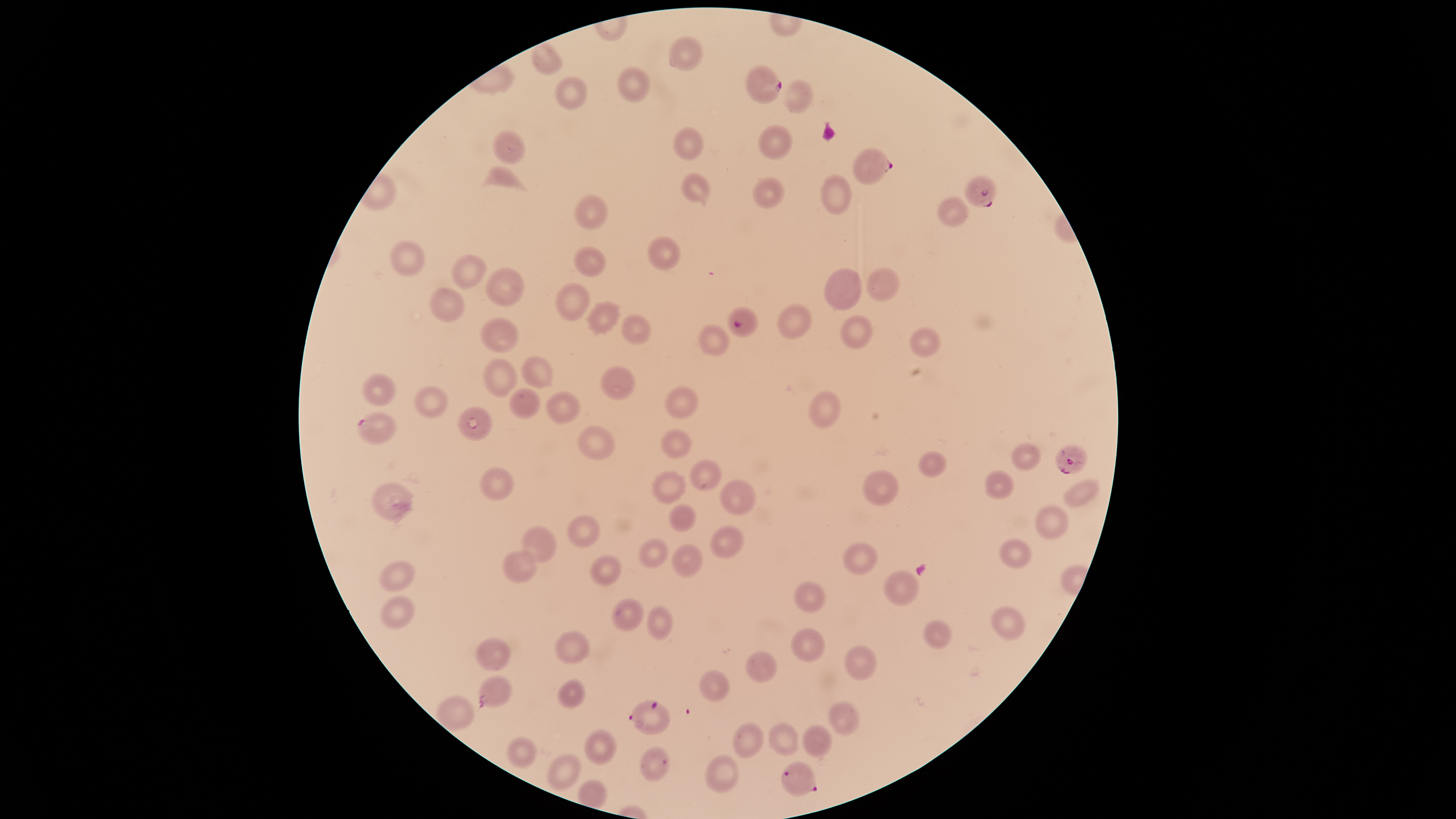

Approximate bounding boxes, in pixels from the top-left corner. Parasitized red blood cells: (left=745, top=64, right=782, bottom=104), (left=852, top=147, right=893, bottom=185), (left=964, top=175, right=997, bottom=207), (left=727, top=306, right=758, bottom=337), (left=357, top=411, right=397, bottom=445), (left=1054, top=444, right=1088, bottom=475), (left=478, top=676, right=512, bottom=708), (left=628, top=699, right=670, bottom=735), (left=781, top=762, right=817, bottom=797). Uninfected red blood cells: (left=668, top=36, right=703, bottom=70), (left=531, top=44, right=562, bottom=75), (left=616, top=66, right=651, bottom=102), (left=554, top=76, right=588, bottom=110), (left=782, top=78, right=815, bottom=114), (left=757, top=124, right=793, bottom=160), (left=671, top=127, right=706, bottom=160), (left=492, top=129, right=524, bottom=163), (left=479, top=165, right=531, bottom=193), (left=681, top=172, right=711, bottom=202), (left=820, top=174, right=852, bottom=215), (left=751, top=177, right=785, bottom=209), (left=573, top=194, right=608, bottom=230), (left=936, top=196, right=969, bottom=227), (left=647, top=236, right=681, bottom=270), (left=389, top=240, right=425, bottom=276), (left=573, top=246, right=606, bottom=277), (left=451, top=254, right=487, bottom=288), (left=486, top=267, right=524, bottom=306), (left=824, top=268, right=862, bottom=310), (left=866, top=268, right=899, bottom=302), (left=554, top=282, right=589, bottom=320), (left=430, top=287, right=465, bottom=322), (left=588, top=302, right=618, bottom=332), (left=776, top=304, right=811, bottom=338), (left=621, top=314, right=650, bottom=344), (left=840, top=315, right=874, bottom=349), (left=480, top=316, right=519, bottom=352), (left=697, top=325, right=730, bottom=356), (left=908, top=327, right=940, bottom=357), (left=521, top=355, right=553, bottom=388), (left=482, top=358, right=516, bottom=396), (left=599, top=365, right=636, bottom=399), (left=362, top=373, right=397, bottom=406), (left=415, top=385, right=448, bottom=418), (left=664, top=385, right=699, bottom=419), (left=509, top=388, right=540, bottom=418), (left=807, top=390, right=841, bottom=428), (left=545, top=391, right=579, bottom=423), (left=457, top=406, right=493, bottom=440), (left=577, top=425, right=614, bottom=460), (left=660, top=429, right=691, bottom=459), (left=1012, top=444, right=1040, bottom=470), (left=918, top=450, right=946, bottom=478), (left=689, top=459, right=722, bottom=490), (left=481, top=467, right=513, bottom=500), (left=862, top=470, right=899, bottom=506), (left=985, top=470, right=1014, bottom=498), (left=652, top=471, right=687, bottom=503), (left=720, top=479, right=756, bottom=515), (left=1063, top=479, right=1098, bottom=506), (left=371, top=482, right=411, bottom=520), (left=669, top=503, right=695, bottom=531), (left=1036, top=503, right=1068, bottom=539), (left=567, top=514, right=599, bottom=547), (left=521, top=526, right=557, bottom=562), (left=709, top=526, right=744, bottom=558), (left=998, top=537, right=1033, bottom=569), (left=637, top=538, right=668, bottom=567), (left=842, top=542, right=878, bottom=574), (left=670, top=543, right=703, bottom=577), (left=502, top=550, right=538, bottom=582), (left=589, top=554, right=621, bottom=586), (left=379, top=560, right=414, bottom=592), (left=883, top=570, right=919, bottom=606), (left=794, top=581, right=826, bottom=612), (left=378, top=595, right=415, bottom=630), (left=611, top=598, right=644, bottom=630), (left=991, top=605, right=1026, bottom=639), (left=646, top=606, right=671, bottom=639), (left=923, top=619, right=952, bottom=648), (left=790, top=627, right=825, bottom=662), (left=554, top=630, right=588, bottom=664), (left=475, top=637, right=511, bottom=672), (left=843, top=644, right=876, bottom=681), (left=745, top=650, right=778, bottom=682), (left=699, top=669, right=729, bottom=700), (left=557, top=678, right=586, bottom=708), (left=438, top=695, right=473, bottom=729), (left=827, top=700, right=860, bottom=735), (left=768, top=721, right=798, bottom=755), (left=731, top=722, right=764, bottom=757), (left=802, top=724, right=831, bottom=757), (left=584, top=730, right=617, bottom=765), (left=506, top=736, right=536, bottom=768), (left=638, top=745, right=670, bottom=782), (left=547, top=754, right=581, bottom=792), (left=705, top=754, right=739, bottom=793). Image is 1456×819 pixels. Thin blood smear. Photographed with a smartphone camera through the microscope eyepiece. Species: Plasmodium falciparum. Giemsa-stained preparation. One field of view of the specimen. The visible region is circular. Presence: malaria parasites detected.